Assess the morphology of the erythrocytes.
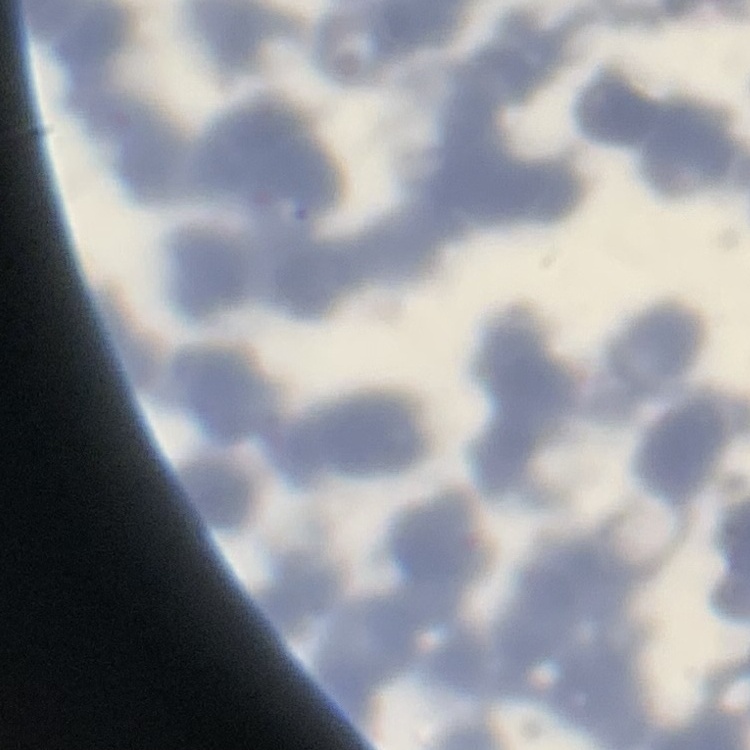
Rouleaux formation.

Summary:
  - Image type: one tile cut from a larger photomicrograph
  - Stain: Field's or Giemsa
  - Preparation: thin blood smear